Outline each Plasmodium ovale-infected red blood cell.
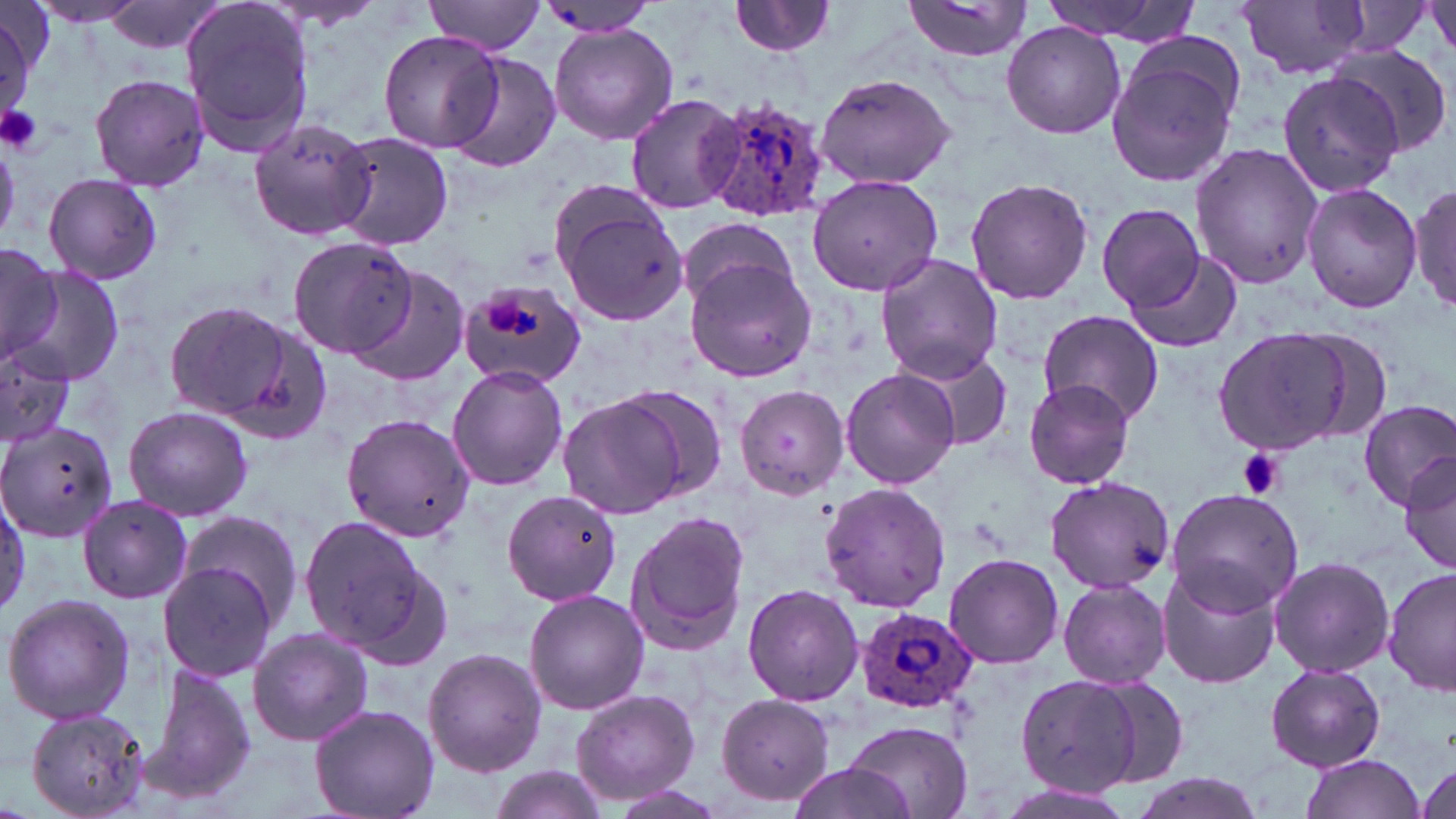
Approximate bounding boxes as (x1, y1, x2, y2) in pixels.
Plasmodium ovale-infected red blood cells: (706, 98, 830, 223), (858, 608, 978, 712).

slide-level diagnosis = Plasmodium ovale
preparation = thin blood film
uninfected red blood cell locations = approximate bounding boxes as (x1, y1, x2, y2) in pixels: (26, 0, 155, 27), (100, 0, 227, 55), (178, 0, 317, 158), (425, 0, 547, 54), (730, 0, 838, 57), (901, 0, 1033, 64), (1039, 0, 1201, 43), (1238, 0, 1373, 80), (1428, 0, 1456, 59), (256, 2, 387, 31), (1, 3, 41, 125), (535, 3, 661, 37), (550, 22, 677, 146), (1000, 22, 1127, 138), (378, 29, 505, 153), (1105, 37, 1246, 190), (1330, 43, 1452, 157), (441, 53, 561, 172), (1277, 68, 1410, 199), (816, 72, 957, 188), (89, 73, 211, 191), (624, 94, 741, 214), (248, 116, 375, 242), (330, 131, 453, 251), (1189, 141, 1324, 291), (42, 173, 162, 284), (806, 174, 945, 297), (964, 176, 1095, 305), (1409, 181, 1455, 312), (1302, 183, 1423, 314), (1095, 204, 1208, 308), (561, 206, 689, 325), (678, 216, 795, 310), (286, 234, 415, 357), (0, 244, 60, 370), (875, 252, 1002, 382), (1127, 252, 1242, 352), (685, 257, 816, 382), (348, 265, 473, 386), (16, 266, 126, 388), (457, 276, 587, 391), (166, 301, 308, 428), (1036, 308, 1163, 425), (1214, 326, 1355, 455), (1295, 327, 1394, 445), (0, 341, 78, 450), (903, 349, 1012, 451), (447, 364, 569, 491), (840, 370, 960, 489), (1023, 379, 1136, 488), (615, 384, 729, 499), (733, 384, 847, 498), (559, 394, 688, 517), (1357, 400, 1456, 508), (122, 405, 253, 521), (341, 413, 476, 543), (0, 421, 117, 544), (1400, 452, 1456, 574), (1042, 475, 1175, 593), (819, 482, 953, 612), (1164, 487, 1305, 611), (501, 489, 622, 605), (77, 494, 192, 603), (180, 507, 305, 639), (626, 509, 751, 654), (298, 517, 437, 658), (943, 552, 1063, 670), (1269, 554, 1395, 677), (155, 561, 282, 681), (1157, 562, 1283, 689), (1383, 567, 1455, 698), (1057, 578, 1172, 687), (741, 583, 865, 706), (524, 591, 650, 716), (2, 593, 135, 725), (247, 627, 372, 746), (423, 648, 547, 775), (142, 661, 257, 804), (1264, 664, 1386, 770), (1012, 676, 1157, 797), (1086, 676, 1193, 789), (569, 687, 701, 805), (715, 694, 839, 806), (310, 704, 441, 819), (25, 709, 150, 818), (841, 718, 974, 818), (1298, 755, 1428, 819), (1412, 759, 1456, 819), (483, 764, 612, 819), (783, 764, 923, 819), (1124, 774, 1265, 819), (593, 785, 734, 819), (995, 786, 1140, 819)
stain = May-Grünwald-Giemsa
field of view = one of a larger specimen
magnification = 1000x
modality = light microscopy
platelet locations = approximate bounding boxes as (x1, y1, x2, y2) in pixels: (0, 104, 43, 155), (482, 294, 525, 338), (1238, 448, 1284, 500)
image size = 1456×819 pixels